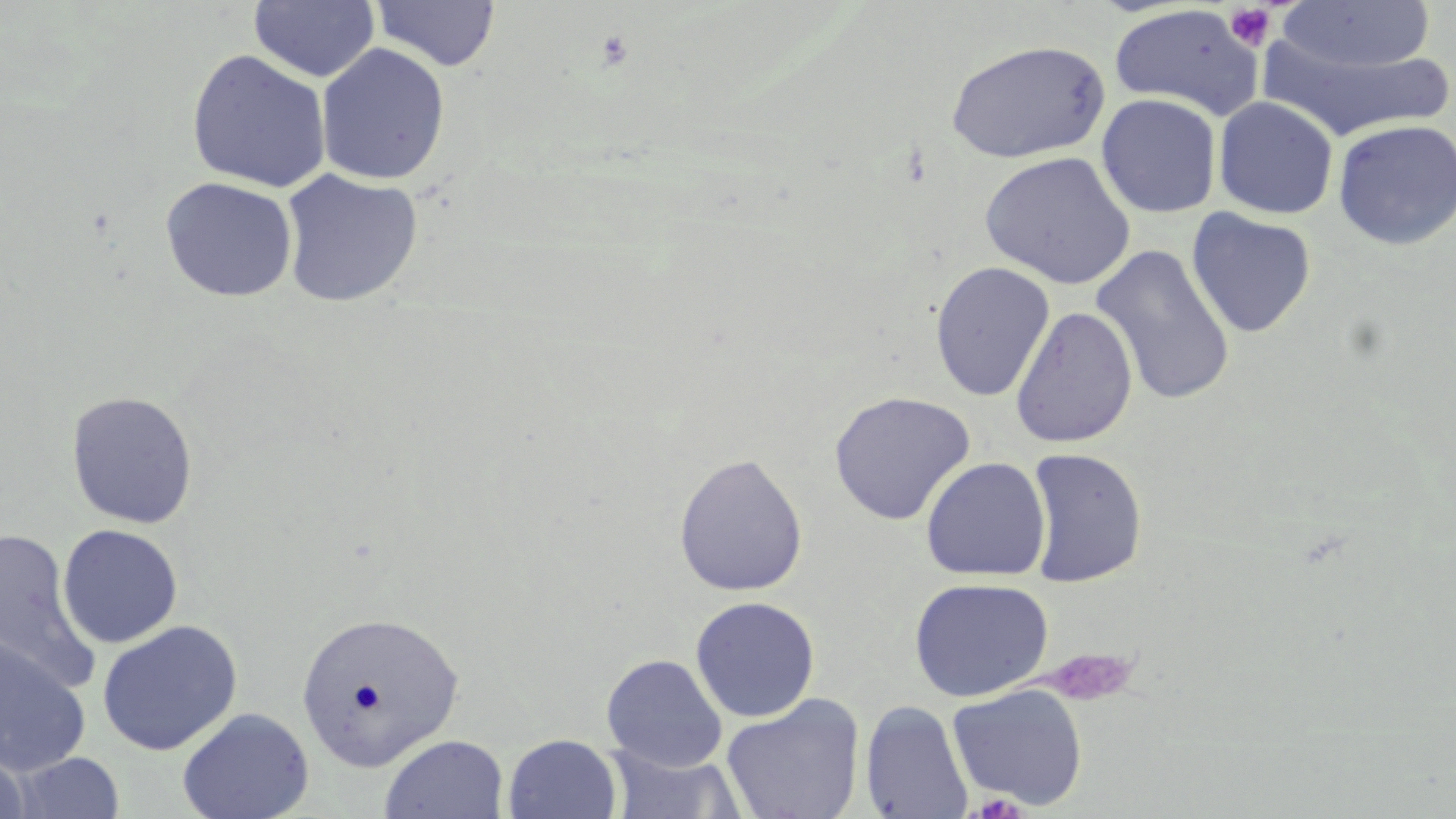

Summary:
  - Coordinate format: approximate bounding boxes as (x1,y1)-(x2,y2) corner pairs in pixels
  - Uninfected red blood cell locations: (250,1)-(379,83), (370,1)-(501,72), (1275,2)-(1437,74), (1108,4)-(1264,120), (1256,33)-(1455,143), (945,39)-(1110,164), (315,43)-(451,185), (186,49)-(331,193), (1097,93)-(1222,218), (1213,96)-(1339,219), (1332,119)-(1456,251), (979,151)-(1136,289), (279,168)-(423,308), (160,176)-(298,302), (1186,207)-(1316,338), (1090,243)-(1237,406), (930,260)-(1055,402), (1010,305)-(1138,448), (65,390)-(199,529), (828,390)-(976,525), (1024,447)-(1148,587), (673,452)-(809,597), (920,456)-(1051,581), (57,524)-(183,648), (0,529)-(103,695), (909,577)-(1054,702), (690,596)-(820,722), (295,607)-(466,770), (97,619)-(243,756), (0,635)-(92,777), (601,653)-(727,772), (946,684)-(1089,810), (721,694)-(866,819), (860,700)-(974,819), (177,707)-(314,819), (502,733)-(622,819), (379,734)-(509,819), (0,743)-(32,819), (602,744)-(748,819), (8,752)-(127,818)
  - Platelet locations: (1225,4)-(1275,51), (1040,648)-(1138,706)
  - Slide-level diagnosis: no evidence of blood parasites
  - Field of view: one of a larger specimen
  - Preparation: thin blood smear
  - Magnification: 1000x
  - Image size: 1456×819 pixels
  - Stain: May-Grünwald-Giemsa
  - Modality: optical microscopy